Locate every Trypanosoma brucei.
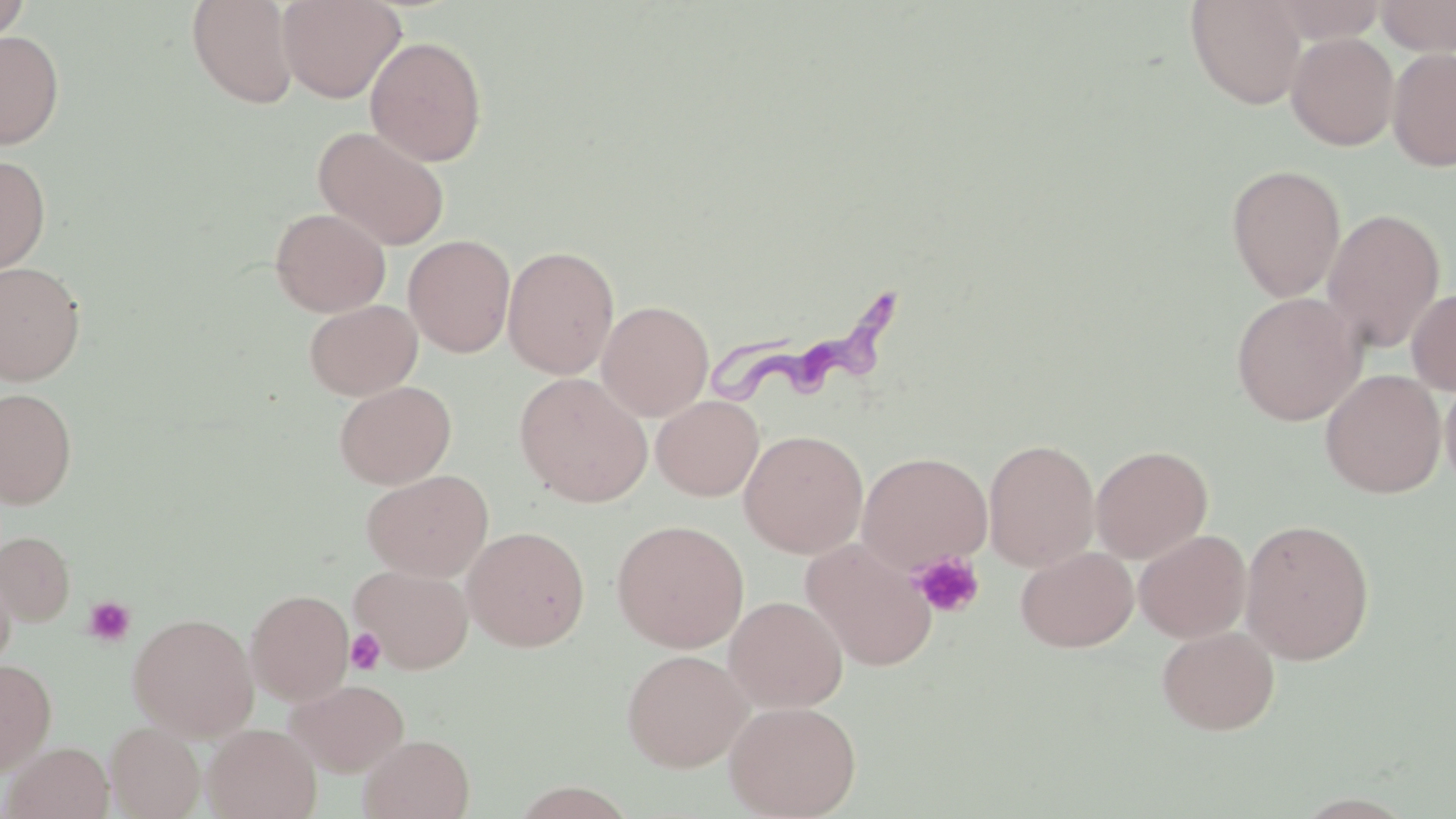
Approximate bounding boxes as named x1/y1/x2/y2 corners in pixels.
Trypanosoma brucei: (x1=708, y1=288, x2=906, y2=408).

Summary:
  - Platelet locations: (x1=910, y1=551, x2=984, y2=618), (x1=82, y1=596, x2=136, y2=647), (x1=345, y1=627, x2=386, y2=675)
  - Uninfected red blood cell locations: (x1=186, y1=0, x2=301, y2=110), (x1=278, y1=0, x2=405, y2=103), (x1=1185, y1=0, x2=1308, y2=110), (x1=1267, y1=0, x2=1386, y2=44), (x1=1376, y1=0, x2=1456, y2=56), (x1=0, y1=1, x2=31, y2=46), (x1=0, y1=29, x2=64, y2=149), (x1=1286, y1=32, x2=1399, y2=150), (x1=365, y1=35, x2=488, y2=166), (x1=1387, y1=47, x2=1456, y2=172), (x1=313, y1=125, x2=451, y2=250), (x1=0, y1=155, x2=52, y2=274), (x1=1226, y1=164, x2=1346, y2=301), (x1=270, y1=207, x2=391, y2=317), (x1=1322, y1=207, x2=1445, y2=353), (x1=404, y1=234, x2=516, y2=357), (x1=502, y1=245, x2=619, y2=379), (x1=0, y1=261, x2=86, y2=386), (x1=1406, y1=287, x2=1456, y2=395), (x1=1231, y1=291, x2=1366, y2=425), (x1=304, y1=299, x2=422, y2=400), (x1=597, y1=299, x2=714, y2=421), (x1=1320, y1=369, x2=1446, y2=498), (x1=1440, y1=370, x2=1456, y2=497), (x1=514, y1=372, x2=653, y2=506), (x1=334, y1=380, x2=456, y2=489), (x1=0, y1=388, x2=77, y2=509), (x1=651, y1=395, x2=764, y2=500), (x1=739, y1=429, x2=868, y2=558), (x1=983, y1=438, x2=1100, y2=572), (x1=1091, y1=444, x2=1213, y2=563), (x1=857, y1=451, x2=993, y2=575), (x1=362, y1=469, x2=494, y2=581), (x1=1239, y1=517, x2=1376, y2=664), (x1=611, y1=519, x2=749, y2=652), (x1=462, y1=525, x2=591, y2=651), (x1=1134, y1=529, x2=1252, y2=643), (x1=0, y1=531, x2=75, y2=624), (x1=802, y1=539, x2=938, y2=671), (x1=1015, y1=546, x2=1138, y2=652), (x1=0, y1=558, x2=16, y2=671), (x1=350, y1=564, x2=474, y2=673), (x1=245, y1=588, x2=355, y2=705), (x1=724, y1=595, x2=848, y2=712), (x1=128, y1=612, x2=259, y2=740), (x1=1156, y1=625, x2=1280, y2=735), (x1=622, y1=648, x2=751, y2=772), (x1=0, y1=659, x2=56, y2=775), (x1=286, y1=679, x2=409, y2=776), (x1=724, y1=700, x2=861, y2=818), (x1=105, y1=721, x2=205, y2=819), (x1=203, y1=724, x2=321, y2=819), (x1=359, y1=733, x2=474, y2=819), (x1=3, y1=741, x2=114, y2=819)
  - Slide-level diagnosis: Trypanosoma brucei
  - Modality: light microscopy
  - Field of view: one of a larger specimen
  - Preparation: thin blood film
  - Stain: May-Grünwald-Giemsa
  - Image size: 1456×819 pixels
  - Magnification: 1000x